Classify this cell by malaria status.
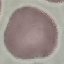
Uninfected.

Summary:
  - Preparation: thin blood smear
  - Capture: smartphone camera at the microscope eyepiece
  - Stain: Giemsa
  - Image type: cell patch, automatically extracted from a larger field of view and resized to 64 × 64 pixels